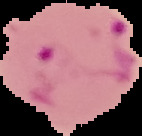
image size = 142×136 pixels
result = malaria parasites detected
preparation = thin blood film
image type = cell region segmented out of the field of view; surrounding area masked to black